Identify the blood parasite species.
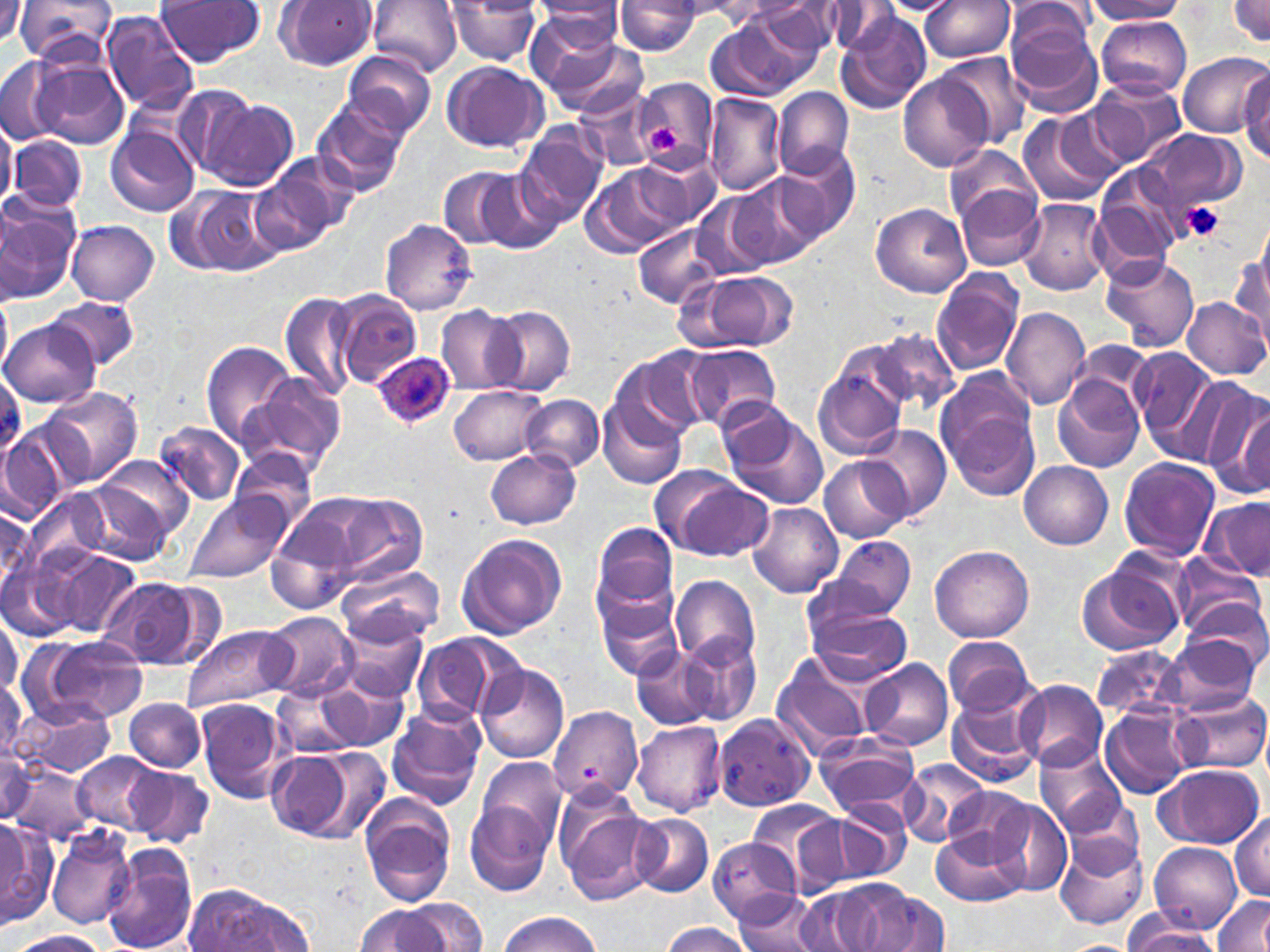

Plasmodium ovale.

uninfected red blood cell locations = approximate bounding boxes as [x1, y1, x2, y2] in pixels: [1, 0, 29, 47], [15, 0, 117, 67], [156, 0, 264, 65], [275, 0, 377, 71], [368, 0, 462, 76], [701, 0, 794, 30], [876, 0, 958, 16], [1087, 0, 1185, 22], [1229, 0, 1270, 44], [614, 1, 702, 56], [760, 1, 846, 57], [921, 1, 1014, 62], [445, 2, 542, 64], [533, 2, 625, 42], [824, 3, 898, 54], [1004, 3, 1099, 51], [715, 9, 823, 99], [101, 10, 199, 114], [1003, 12, 1104, 118], [1095, 14, 1193, 98], [836, 16, 930, 115], [533, 28, 645, 117], [342, 51, 436, 139], [936, 51, 1034, 148], [1179, 54, 1268, 137], [0, 56, 67, 144], [26, 56, 130, 151], [442, 60, 547, 153], [1239, 67, 1270, 164], [898, 72, 994, 172], [634, 77, 717, 171], [1087, 78, 1186, 169], [573, 85, 658, 171], [774, 88, 853, 179], [704, 93, 786, 197], [199, 97, 298, 192], [312, 97, 409, 198], [1055, 109, 1132, 185], [1016, 112, 1116, 209], [0, 121, 20, 207], [105, 125, 197, 216], [513, 126, 608, 227], [1140, 128, 1246, 215], [9, 134, 87, 212], [945, 144, 1039, 231], [779, 149, 859, 243], [264, 151, 362, 238], [635, 153, 721, 230], [1094, 164, 1188, 269], [583, 165, 685, 259], [439, 166, 524, 251], [254, 171, 336, 258], [476, 172, 561, 253], [730, 174, 824, 268], [956, 184, 1045, 270], [190, 186, 283, 275], [0, 189, 82, 304], [692, 192, 779, 281], [1018, 198, 1110, 295], [870, 202, 971, 297], [380, 217, 477, 314], [67, 220, 159, 305], [634, 223, 725, 308], [1233, 248, 1270, 344], [1101, 254, 1200, 353], [683, 269, 800, 353], [930, 269, 1025, 375], [1104, 283, 1198, 440], [331, 289, 423, 388], [279, 290, 359, 399], [0, 293, 12, 375], [51, 297, 137, 372], [1182, 297, 1270, 380], [436, 306, 525, 396], [489, 306, 575, 395], [1001, 306, 1090, 410], [2, 321, 100, 408], [867, 329, 958, 411], [201, 341, 297, 448], [684, 344, 783, 427], [1129, 346, 1222, 456], [613, 349, 710, 444], [814, 349, 913, 459], [1144, 365, 1263, 474], [243, 373, 347, 478], [1054, 374, 1145, 473], [1190, 381, 1270, 492], [450, 383, 549, 464], [44, 385, 141, 486], [939, 387, 1043, 503], [521, 395, 603, 472], [599, 395, 687, 489], [720, 405, 828, 511], [1, 420, 84, 517], [154, 421, 246, 507], [862, 426, 950, 521], [486, 447, 580, 529], [230, 448, 319, 534], [89, 454, 193, 554], [820, 457, 909, 544], [1118, 457, 1220, 562], [1020, 462, 1114, 549], [652, 467, 772, 563], [27, 490, 110, 569], [318, 493, 430, 585], [185, 495, 292, 585], [1202, 497, 1270, 581], [747, 503, 843, 598], [0, 506, 43, 594], [268, 511, 361, 615], [591, 521, 679, 619], [456, 532, 567, 640], [829, 535, 915, 619], [931, 545, 1033, 643], [53, 549, 142, 640], [1171, 553, 1264, 639], [3, 557, 78, 641], [1077, 560, 1186, 658], [333, 562, 445, 648], [670, 574, 760, 669], [101, 579, 196, 668], [596, 594, 683, 681], [1184, 596, 1268, 669], [807, 605, 914, 687], [1, 610, 21, 698], [260, 612, 356, 703], [344, 622, 431, 701], [182, 624, 293, 713], [677, 631, 762, 726], [412, 632, 522, 725], [28, 635, 148, 724], [943, 635, 1036, 719], [1164, 635, 1262, 715], [1092, 645, 1190, 721], [634, 647, 717, 732], [771, 655, 875, 760], [859, 659, 953, 750], [476, 664, 569, 764], [0, 677, 27, 766], [314, 678, 409, 751], [1014, 680, 1108, 771], [274, 684, 360, 760], [1173, 692, 1269, 773], [16, 697, 117, 780], [948, 697, 1041, 788], [124, 698, 207, 771], [196, 698, 290, 804], [550, 702, 644, 813], [387, 703, 485, 808], [1102, 705, 1196, 798], [713, 711, 816, 811], [632, 720, 726, 816], [816, 733, 924, 819], [1, 745, 38, 826], [1034, 745, 1126, 835], [265, 748, 381, 840], [71, 754, 162, 834], [474, 757, 567, 848], [896, 758, 994, 848], [122, 763, 214, 848], [10, 764, 95, 842], [1154, 765, 1265, 848], [942, 787, 1034, 864], [358, 793, 457, 907], [556, 794, 660, 904], [1059, 795, 1145, 881], [748, 799, 845, 884], [988, 799, 1073, 895], [831, 800, 913, 882], [465, 802, 555, 895], [1231, 812, 1270, 901], [631, 814, 714, 898], [0, 819, 54, 930], [934, 825, 1026, 907], [46, 827, 134, 928], [1055, 835, 1149, 931], [708, 838, 802, 923], [1150, 841, 1242, 934], [101, 844, 198, 952], [815, 879, 948, 952], [185, 885, 306, 951], [731, 890, 826, 951], [794, 890, 874, 950], [1213, 895, 1270, 949], [403, 898, 487, 951], [358, 906, 450, 952], [496, 912, 603, 951], [1123, 916, 1218, 951], [659, 920, 754, 951], [7, 931, 109, 952], [1054, 939, 1138, 951]
Plasmodium ovale-infected red blood cell locations = approximate bounding boxes as [x1, y1, x2, y2] in pixels: [371, 352, 455, 429]
field of view = single
image size = 1270×952 pixels
platelet locations = approximate bounding boxes as [x1, y1, x2, y2] in pixels: [647, 125, 681, 153], [1180, 201, 1225, 242]
preparation = thin blood film
magnification = 1000x
modality = light microscopy
stain = May-Grünwald-Giemsa